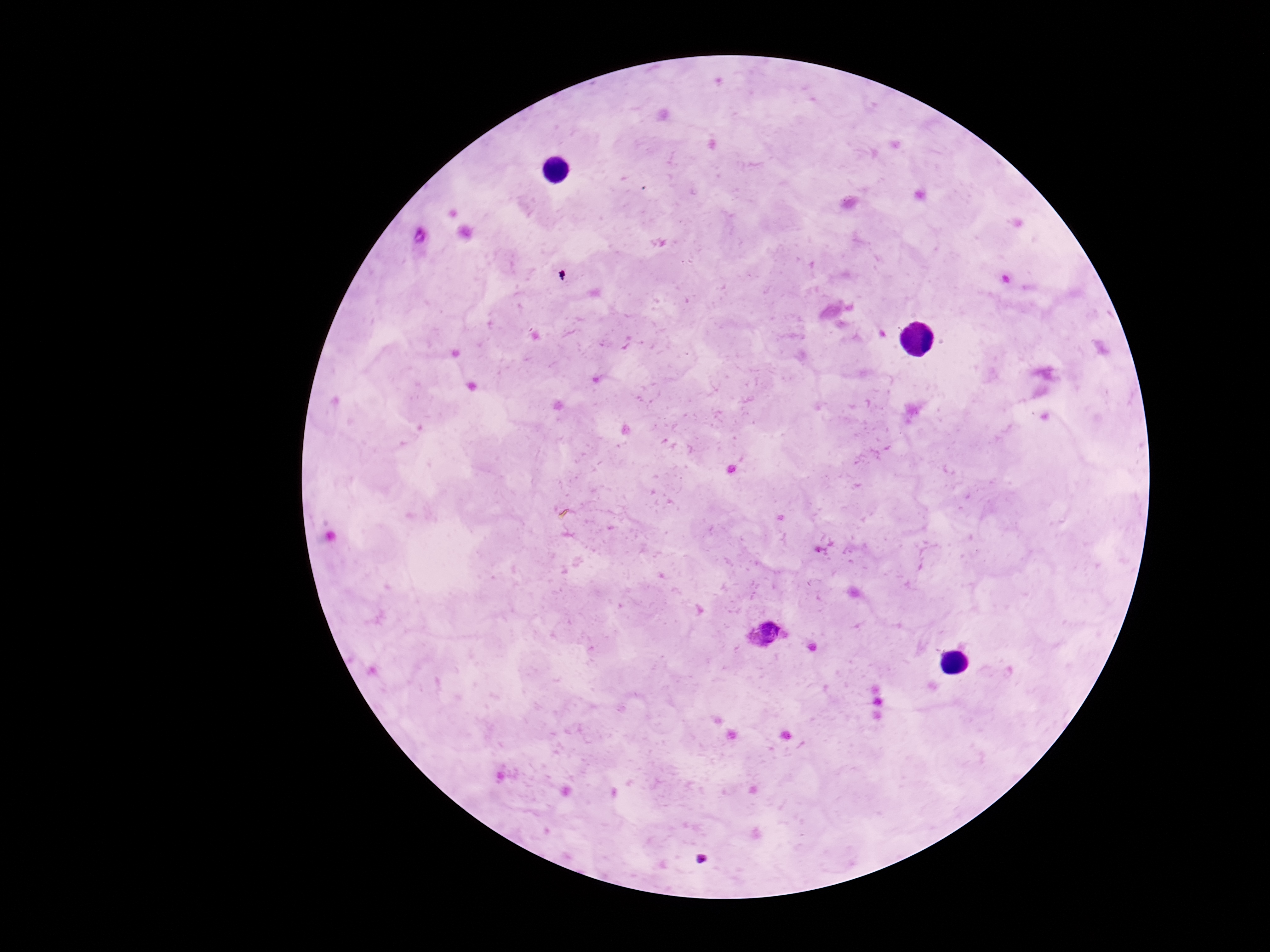

Approximate object centers, in pixels from the top-left corner. Plasmodium parasite locations: (x=419, y=239), (x=765, y=635). Giemsa stain. Thick peripheral-blood smear. One field from this slide. Photographed through the microscope eyepiece with a smartphone camera. Patient malaria status: positive. 100x magnification. Image is 1270×952 pixels.